State which parasite is depicted.
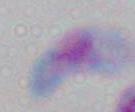

This is Toxoplasma gondii.

Micrograph. 1000x magnification.